Outline each uninfected red blood cell.
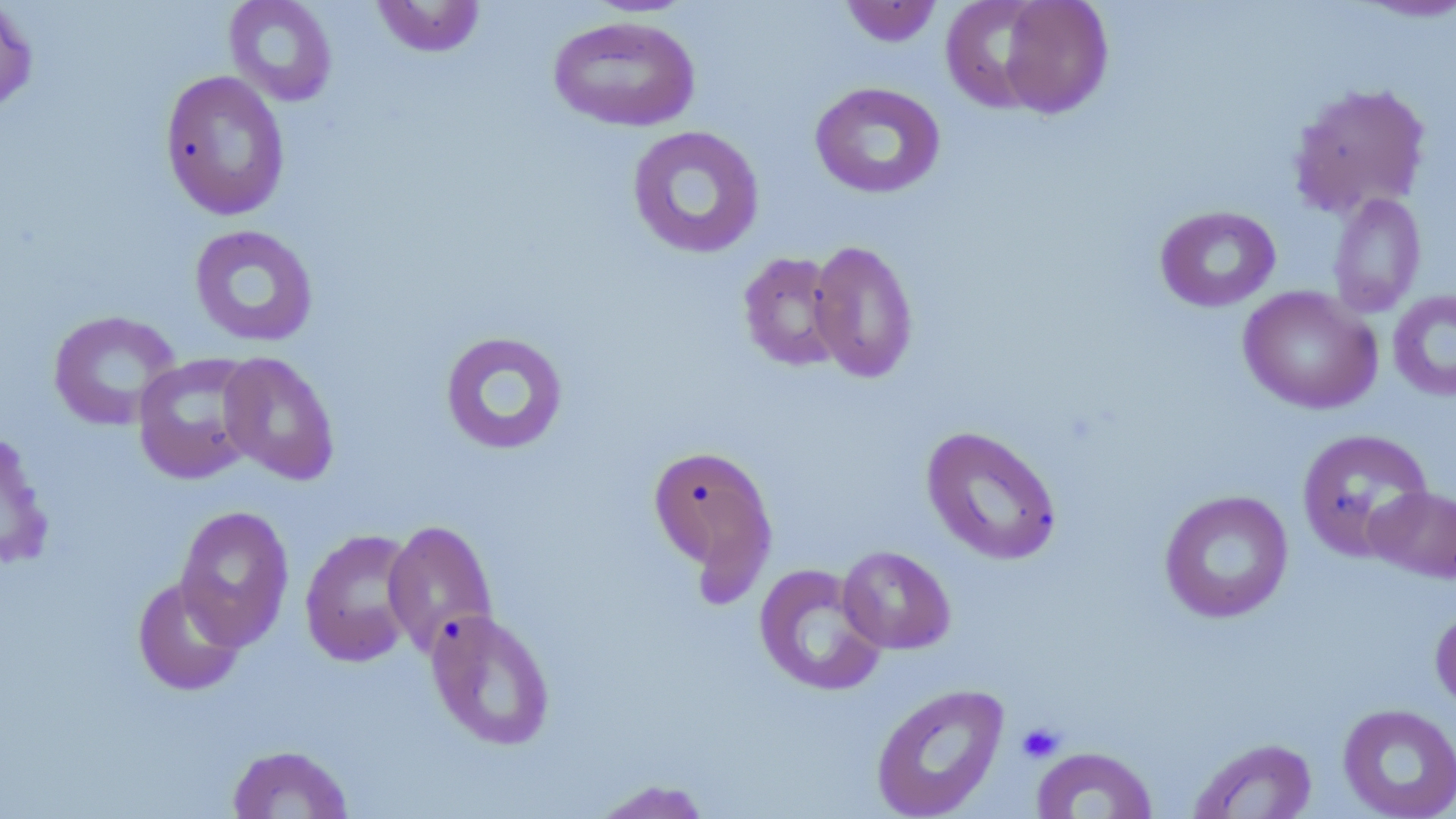

Approximate bounding boxes as (x1, y1, x2, y2) in pixels.
Uninfected red blood cells: (0, 0, 39, 119), (223, 0, 338, 107), (370, 0, 487, 58), (995, 0, 1114, 119), (839, 1, 943, 47), (1346, 1, 1456, 24), (547, 15, 701, 132), (159, 70, 291, 221), (1286, 80, 1433, 219), (809, 81, 946, 200), (626, 125, 765, 259), (1327, 192, 1426, 318), (1154, 205, 1281, 312), (189, 224, 319, 347), (809, 239, 919, 383), (738, 251, 846, 372), (1238, 286, 1383, 414), (1387, 289, 1456, 401), (47, 309, 181, 430), (439, 330, 569, 456), (219, 352, 339, 485), (132, 353, 263, 484), (1, 423, 54, 575), (921, 425, 1063, 566), (1296, 429, 1434, 561), (647, 442, 779, 595), (1366, 486, 1456, 584), (1159, 489, 1294, 624), (174, 504, 294, 650), (383, 519, 498, 657), (299, 528, 422, 667), (837, 545, 956, 654), (753, 562, 887, 698), (131, 575, 248, 697), (1430, 603, 1456, 715), (426, 609, 556, 751), (869, 682, 1010, 819), (1337, 703, 1456, 819), (1189, 737, 1318, 818), (226, 743, 354, 818), (1031, 746, 1158, 818), (588, 779, 716, 818).

Summary:
  - Platelet locations: (1016, 721, 1066, 764)
  - Slide-level diagnosis: no evidence of blood parasites
  - Image size: 1456×819 pixels
  - Modality: light microscopy
  - Stain: May-Grünwald-Giemsa
  - Magnification: 1000x
  - Preparation: thin blood smear
  - Field of view: single